Assess the morphology of the red blood cells.
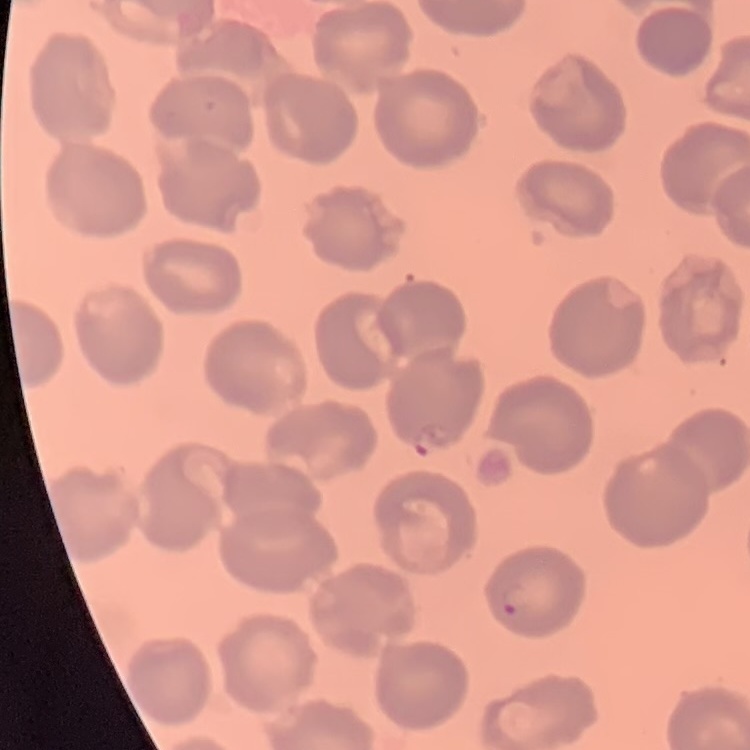

No rouleaux formation.

One tile cut from a larger photomicrograph. Thin blood smear. Stained with either Field's or Giemsa.